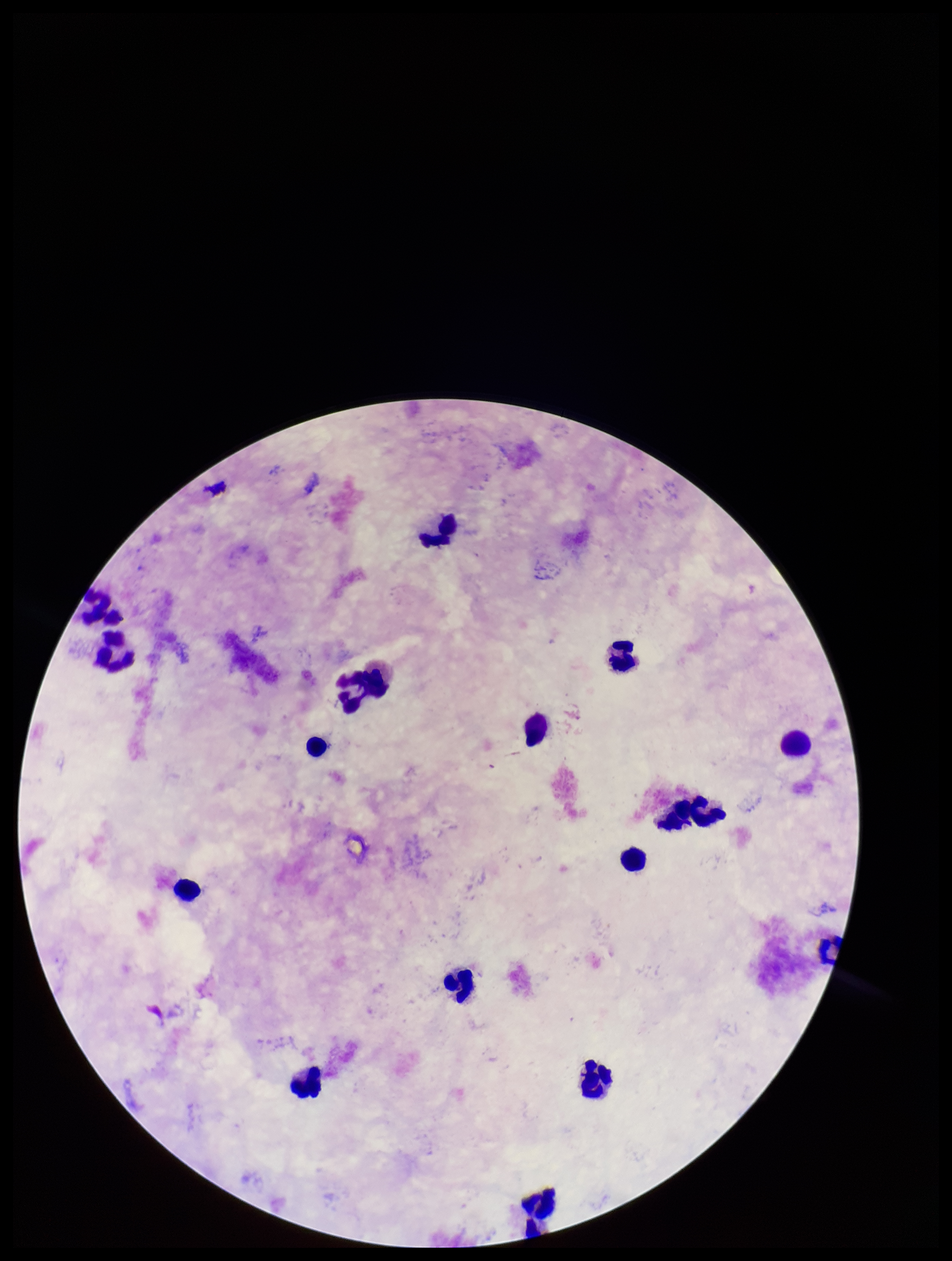

Summary:
  - Plasmodium parasites: none detected
  - Field of view: single
  - Preparation: thick
  - Parasite count: 0
  - Patient malaria status: negative
  - Image size: 952×1261 pixels
  - Leukocyte count: 16
  - Capture: smartphone photograph through the microscope eyepiece
  - Stain: Giemsa